Name the blood parasite species.
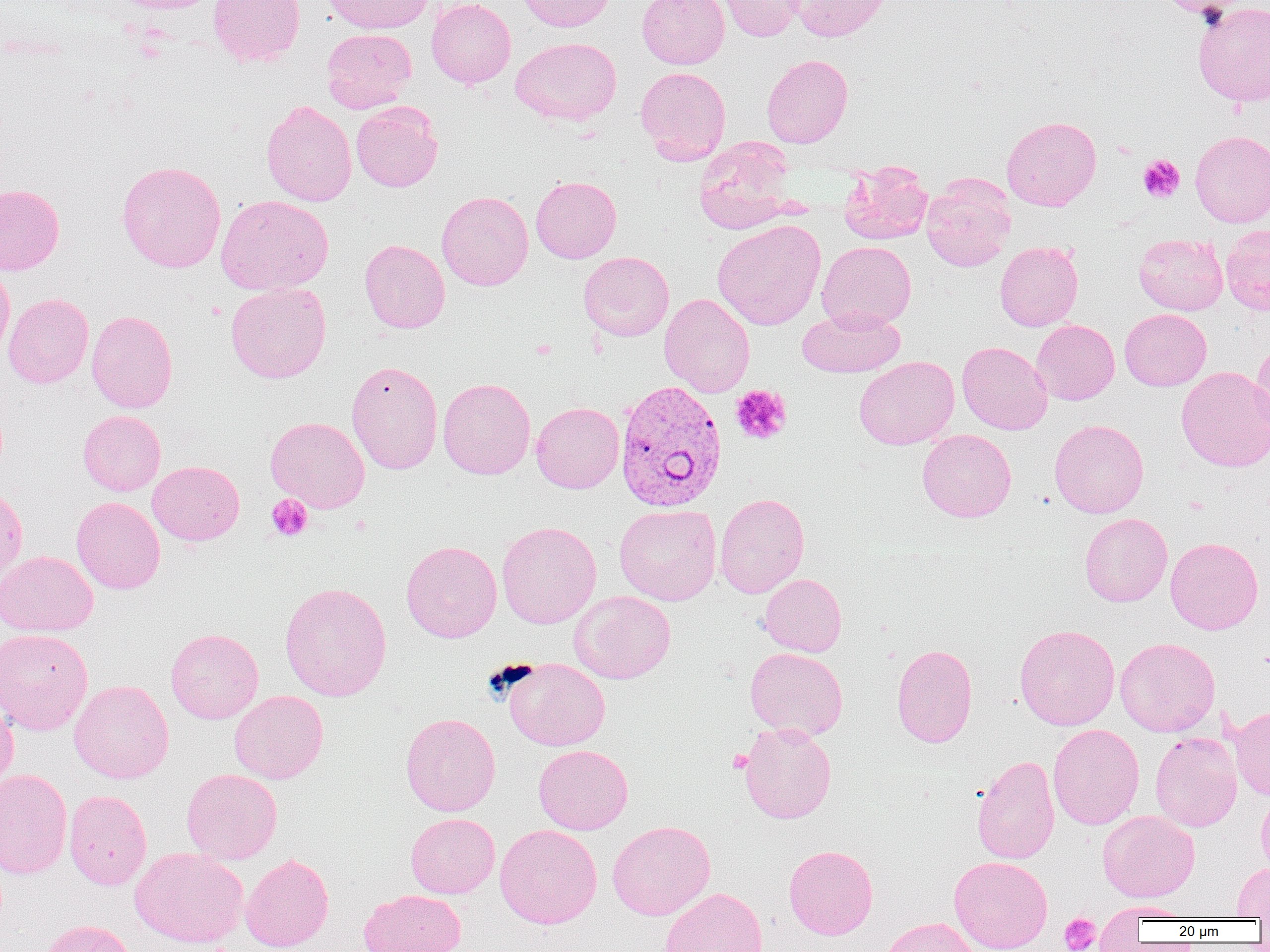

Plasmodium vivax.

platelet locations = approximate bounding boxes as (x1,y1)-(x2,y2) corner pairs in pixels: (1138,154)-(1185,203), (730,384)-(792,444), (266,494)-(313,541), (727,750)-(753,772), (1059,913)-(1100,952)
modality = optical microscopy
magnification = 1000x
image size = 1270×952 pixels
Plasmodium vivax-infected red blood cell locations = approximate bounding boxes as (x1,y1)-(x2,y2) corner pairs in pixels: (615,378)-(728,513)
preparation = thin blood smear
uninfected red blood cell locations = approximate bounding boxes as (x1,y1)-(x2,y2) corner pairs in pixels: (111,0)-(223,13), (208,0)-(305,67), (321,0)-(433,34), (426,0)-(516,88), (513,0)-(614,32), (637,0)-(729,69), (716,0)-(806,41), (788,0)-(893,42), (1159,0)-(1249,19), (1192,2)-(1270,107), (321,29)-(417,113), (511,37)-(622,125), (761,54)-(853,147), (635,66)-(731,164), (261,100)-(357,206), (351,101)-(443,192), (1002,115)-(1102,211), (1190,130)-(1270,227), (694,138)-(797,234), (116,160)-(226,273), (839,161)-(933,245), (531,176)-(621,263), (921,176)-(1015,271), (0,183)-(65,275), (436,191)-(533,291), (215,195)-(333,295), (712,219)-(826,330), (1220,224)-(1270,315), (1134,234)-(1228,315), (360,239)-(450,333), (817,241)-(916,330), (995,242)-(1083,331), (578,251)-(674,341), (0,262)-(15,365), (226,282)-(331,383), (4,292)-(93,388), (659,293)-(755,397), (797,306)-(905,377), (1120,308)-(1211,391), (87,310)-(178,413), (1031,319)-(1119,405), (1250,338)-(1270,443), (957,341)-(1052,434), (853,356)-(959,450), (346,360)-(443,474), (1176,366)-(1270,472), (438,377)-(535,479), (531,402)-(624,493), (77,409)-(166,496), (265,416)-(370,513), (1049,419)-(1149,518), (917,429)-(1016,522), (147,460)-(245,545), (0,486)-(27,589), (714,492)-(809,598), (71,496)-(166,594), (614,504)-(721,605), (1079,513)-(1173,607), (497,521)-(601,629), (1165,537)-(1264,634), (401,540)-(502,642), (0,550)-(98,636), (760,574)-(847,657), (279,581)-(392,702), (569,591)-(676,684), (1014,624)-(1119,730), (165,628)-(264,723), (0,629)-(93,734), (1115,637)-(1220,736), (892,644)-(978,747), (745,647)-(848,740), (503,658)-(610,751), (69,680)-(173,783), (229,691)-(328,783), (0,695)-(18,792), (1230,706)-(1270,800), (400,712)-(501,816), (739,722)-(836,824), (1048,724)-(1144,829), (1149,731)-(1242,832), (533,744)-(633,835), (972,755)-(1060,864), (0,768)-(73,879), (181,768)-(282,864), (1256,788)-(1270,879), (64,789)-(152,890), (1098,810)-(1199,902), (405,813)-(500,898), (607,820)-(715,920), (495,824)-(602,928), (784,845)-(878,939), (130,847)-(248,948), (240,852)-(334,951), (949,855)-(1053,952), (1233,862)-(1270,919), (660,886)-(768,952), (358,889)-(467,952), (1097,900)-(1194,921), (880,917)-(982,952), (39,919)-(137,952)
field of view = one of a larger specimen